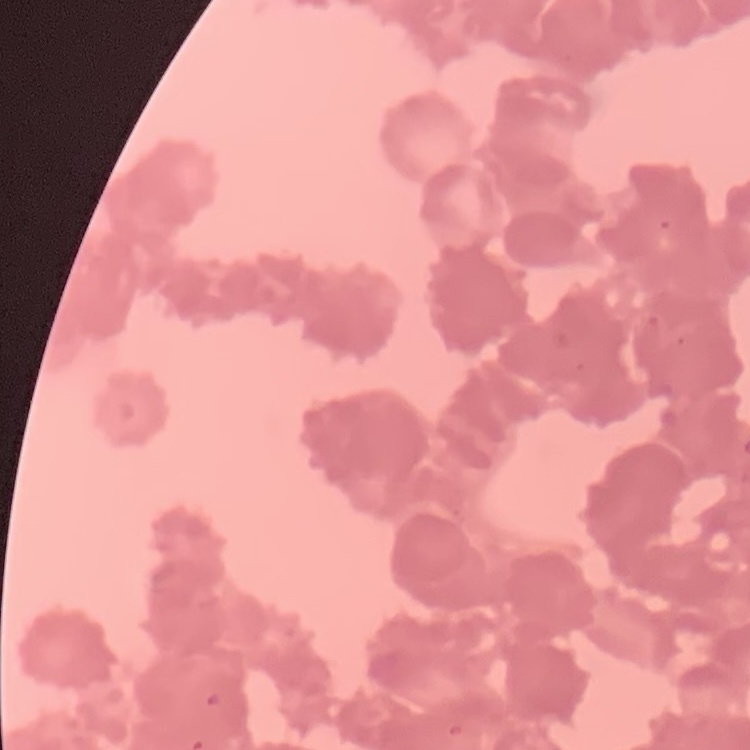
The erythrocytes exhibit rouleaux formation. One tile cut from a larger photomicrograph. Thin blood smear. Field's or Giemsa stain.